Comment on the morphology of the erythrocytes.
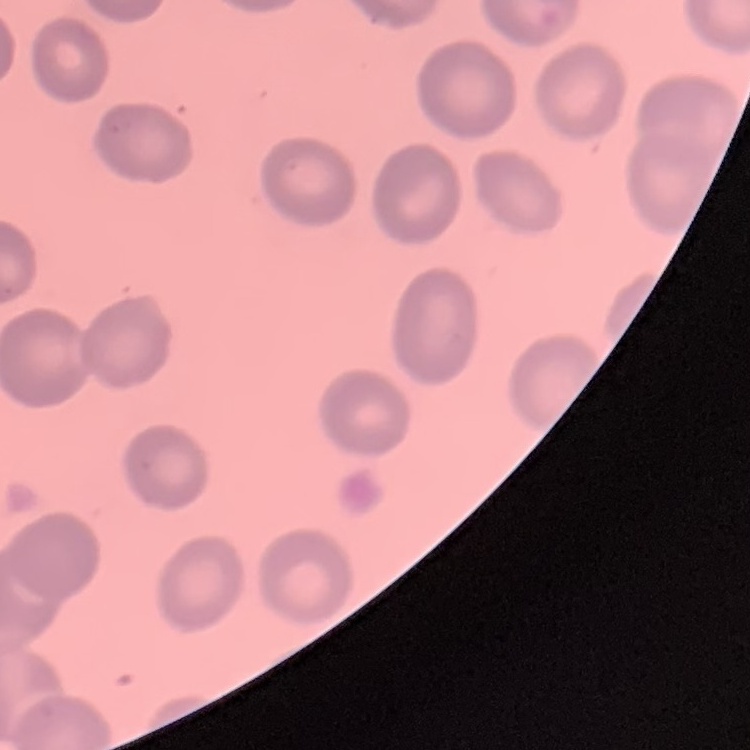

No rouleaux formation.

Thin blood smear. Square crop of a larger photomicrograph. Stained with either Field's or Giemsa.